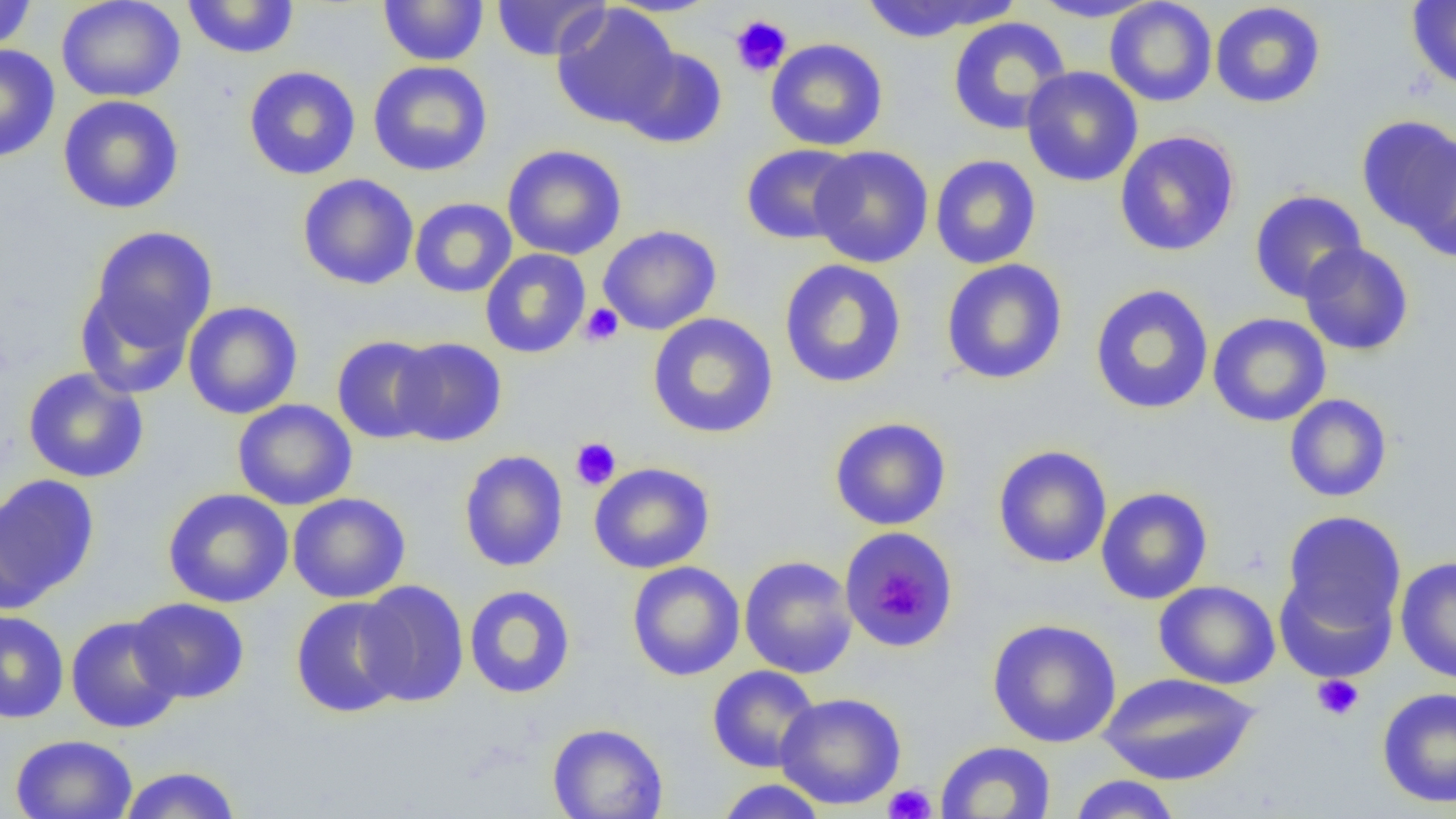

slide-level diagnosis = no evidence of blood parasites
modality = optical microscopy
image size = 1456×819 pixels
magnification = 1000x
uninfected red blood cell locations = approximate bounding boxes as [x1, y1, x2, y2] in pixels: [0, 0, 37, 52], [56, 0, 186, 103], [377, 0, 490, 66], [491, 0, 611, 61], [858, 0, 1008, 43], [1028, 0, 1165, 22], [1104, 0, 1217, 107], [182, 1, 300, 59], [1407, 1, 1456, 93], [1210, 2, 1326, 108], [551, 3, 681, 129], [947, 17, 1072, 135], [765, 38, 888, 152], [0, 45, 60, 163], [619, 46, 729, 150], [368, 60, 493, 176], [243, 65, 361, 180], [1021, 66, 1143, 187], [57, 95, 185, 214], [1356, 114, 1456, 243], [1114, 130, 1241, 257], [1404, 133, 1456, 264], [502, 144, 627, 260], [740, 144, 860, 246], [809, 146, 934, 268], [930, 155, 1041, 269], [297, 173, 419, 290], [1249, 189, 1367, 302], [409, 197, 517, 298], [597, 225, 721, 335], [86, 226, 218, 353], [1298, 242, 1414, 356], [480, 249, 591, 359], [778, 259, 908, 389], [940, 259, 1068, 385], [75, 283, 196, 399], [1088, 284, 1215, 415], [183, 301, 302, 419], [55, 309, 182, 461], [647, 312, 778, 439], [1207, 312, 1332, 427], [331, 335, 441, 445], [392, 337, 507, 447], [22, 367, 149, 483], [1284, 394, 1393, 502], [232, 399, 358, 510], [829, 416, 952, 531], [992, 445, 1112, 569], [458, 450, 568, 572], [589, 462, 715, 574], [0, 474, 100, 607], [1096, 486, 1213, 605], [162, 487, 294, 608], [287, 492, 411, 603], [1280, 511, 1407, 638], [839, 526, 960, 654], [739, 555, 858, 678], [1395, 556, 1456, 683], [627, 561, 745, 681], [1274, 566, 1398, 683], [356, 580, 469, 707], [1154, 580, 1280, 689], [463, 585, 577, 699], [290, 596, 410, 718], [128, 597, 250, 704], [0, 610, 69, 723], [65, 615, 185, 734], [987, 618, 1122, 747], [706, 664, 821, 773], [1098, 672, 1260, 785], [1376, 686, 1456, 809], [775, 691, 907, 810], [547, 723, 668, 818], [10, 733, 138, 819], [935, 741, 1056, 818], [117, 766, 242, 819], [1067, 774, 1183, 818], [714, 778, 829, 819]
field of view = one of a larger specimen
preparation = thin blood film
platelet locations = approximate bounding boxes as [x1, y1, x2, y2] in pixels: [729, 14, 793, 78], [580, 303, 623, 346], [570, 438, 621, 490], [879, 578, 922, 620], [1312, 674, 1364, 721], [883, 783, 937, 819]